Classify this cell by malaria status.
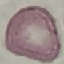
It is uninfected.

Summary:
  - Image type: automatically extracted cell patch, resized to 64 × 64 pixels
  - Preparation: thin smear
  - Stain: Giemsa
  - Capture: smartphone through the microscope eyepiece